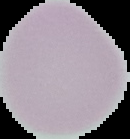
image size = 130×139 pixels
preparation = thin blood smear
malaria status = uninfected
image type = segmented cell region with the area outside set to black